Identify the blood parasite species.
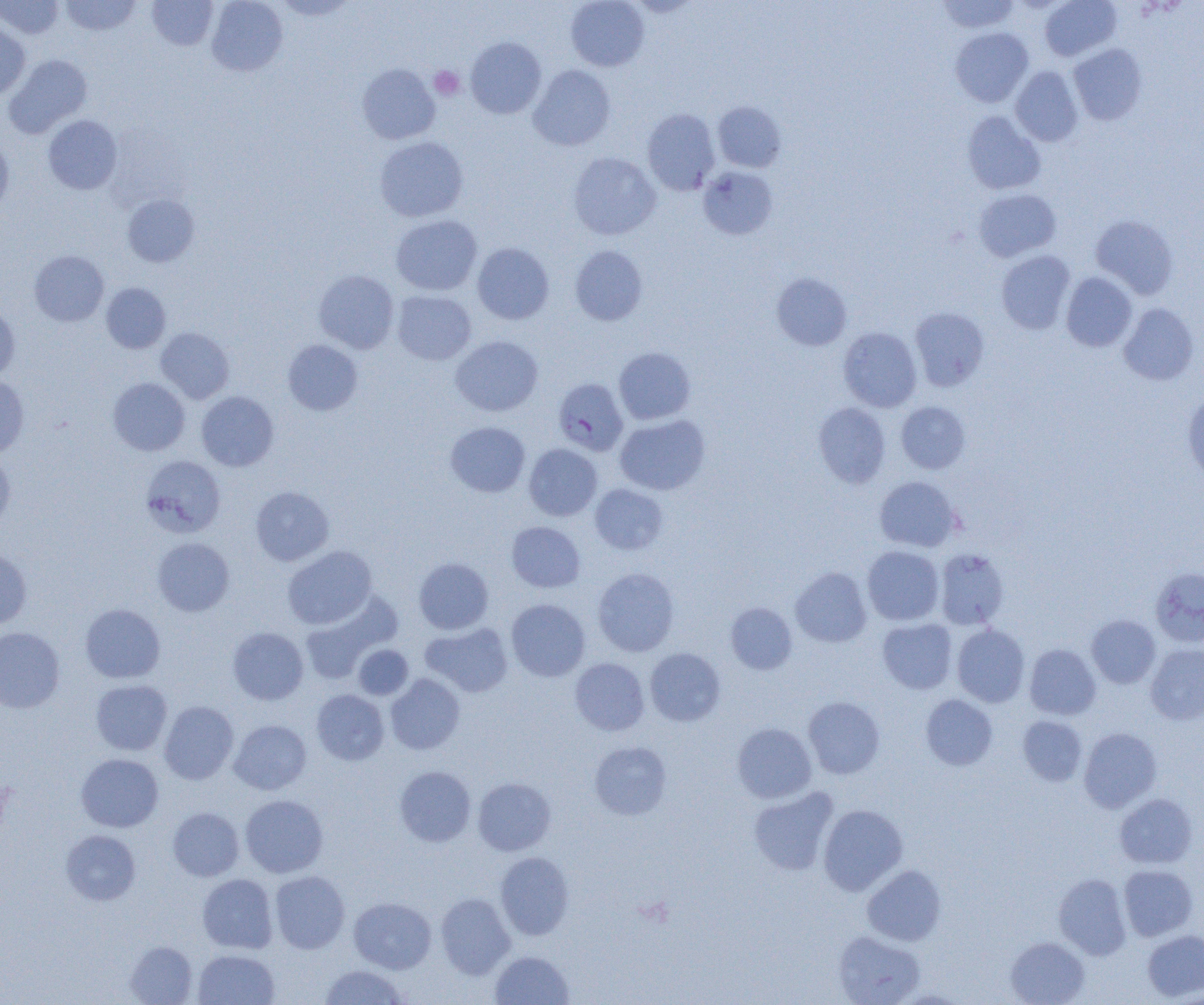

Plasmodium falciparum.

modality = optical microscopy
Plasmodium falciparum-infected red blood cell locations = approximate bounding boxes as (x1,y1)-(x2,y2) corner pairs in pixels: (553,378)-(628,456)
preparation = thin blood smear
platelet locations = approximate bounding boxes as (x1,y1)-(x2,y2) corner pairs in pixels: (429,66)-(464,100)
uninfected red blood cell locations = approximate bounding boxes as (x1,y1)-(x2,y2) corner pairs in pixels: (0,0)-(63,39), (59,0)-(142,36), (147,0)-(217,50), (206,0)-(288,76), (565,0)-(650,71), (936,0)-(1020,33), (1039,0)-(1121,61), (0,22)-(31,100), (950,27)-(1033,107), (466,37)-(546,119), (1069,43)-(1147,126), (4,54)-(92,138), (357,63)-(441,144), (528,65)-(616,151), (1010,66)-(1082,146), (713,101)-(786,173), (642,108)-(720,194), (962,111)-(1046,195), (43,115)-(122,194), (0,136)-(14,216), (375,136)-(468,221), (568,152)-(661,240), (698,166)-(778,240), (973,188)-(1061,262), (122,194)-(199,267), (1090,214)-(1179,299), (391,215)-(482,296), (473,243)-(554,324), (570,245)-(648,325), (30,250)-(109,326), (996,250)-(1075,334), (313,270)-(399,354), (771,272)-(852,351), (1061,272)-(1137,352), (101,283)-(170,353), (393,291)-(476,365), (1118,303)-(1199,385), (0,304)-(20,382), (910,307)-(989,391), (155,327)-(234,404), (838,327)-(922,412), (451,336)-(543,416), (283,339)-(363,415), (613,347)-(696,425), (0,375)-(29,457), (108,377)-(190,455), (1182,390)-(1204,485), (197,391)-(279,471), (896,401)-(970,474), (813,402)-(891,488), (615,415)-(710,495), (445,421)-(530,497), (524,443)-(602,521), (0,453)-(15,536), (141,455)-(226,538), (874,476)-(962,552), (590,484)-(668,555), (250,486)-(334,566), (506,521)-(586,593), (152,537)-(234,616), (282,545)-(377,629), (862,545)-(944,625), (0,549)-(32,629), (934,549)-(1009,630), (414,557)-(493,634), (791,567)-(871,647), (1150,567)-(1204,647), (593,568)-(679,657), (300,595)-(398,683), (506,599)-(590,682), (725,602)-(797,675), (80,603)-(165,683), (1086,615)-(1160,688), (878,619)-(957,694), (421,623)-(513,697), (952,624)-(1030,707), (0,627)-(65,712), (227,627)-(308,705), (353,644)-(413,700), (1025,644)-(1101,719), (1146,644)-(1204,725), (645,648)-(725,726), (570,658)-(649,735), (385,674)-(465,755), (90,679)-(172,755), (311,689)-(389,765), (921,694)-(998,770), (803,696)-(885,779), (159,701)-(238,784), (1018,715)-(1087,786), (229,719)-(311,794), (732,723)-(816,803), (1079,728)-(1162,812), (589,741)-(671,819), (76,754)-(163,832), (394,766)-(476,846), (473,777)-(556,855), (748,787)-(838,875), (1115,793)-(1197,869), (240,795)-(328,878), (818,804)-(908,895), (168,807)-(244,881), (61,829)-(141,905), (495,852)-(574,940), (862,864)-(946,946), (1118,864)-(1198,941), (270,871)-(350,954), (1053,873)-(1131,959), (197,874)-(278,953), (436,892)-(515,979), (349,897)-(436,973), (1142,929)-(1204,1001), (833,930)-(924,1005), (1005,937)-(1089,1005), (125,941)-(198,1005), (193,949)-(279,1005), (490,951)-(574,1005), (319,965)-(409,1005)
field of view = single
image size = 1204×1005 pixels
magnification = 1000x